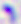
magnification = 400x
modality = photomicrograph
identification = Toxoplasma gondii